Report the malaria status of this cell.
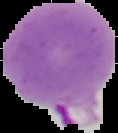

Parasitized.

Summary:
  - Image size: 118×133 pixels
  - Image type: segmented cell region with the area outside set to black
  - Preparation: thin blood smear